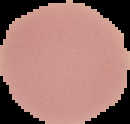

From a thin blood film. Result: no malaria parasites seen. The area outside the segmented cell region is set to black. Image is 130×124 pixels.